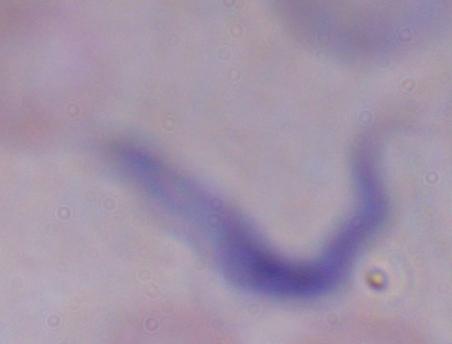
{
  "identification": "trypanosome",
  "modality": "micrograph",
  "magnification": "1000x"
}